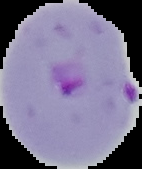

image size = 142×169 pixels
image type = segmented cell region with the area outside set to black
preparation = thin blood film
malaria status = parasitized